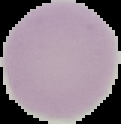

Malaria status: uninfected. Image is 121×124 pixels. The area outside the segmented cell region is set to black. From a thin blood smear.